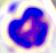
Summary:
  - Identification: leukocyte
  - Modality: micrograph
  - Magnification: 400x